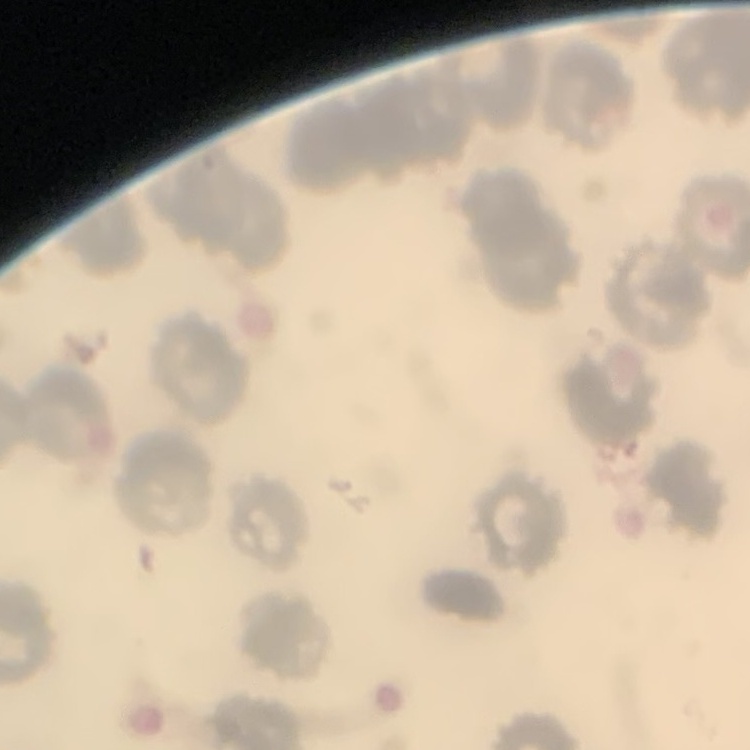
{
  "erythrocyte_morphology": "no rouleaux formation",
  "image_type": "one tile cut from a larger photomicrograph",
  "preparation": "thin blood smear",
  "stain": "Field's or Giemsa"
}